Outline each blood parasite and name the species.
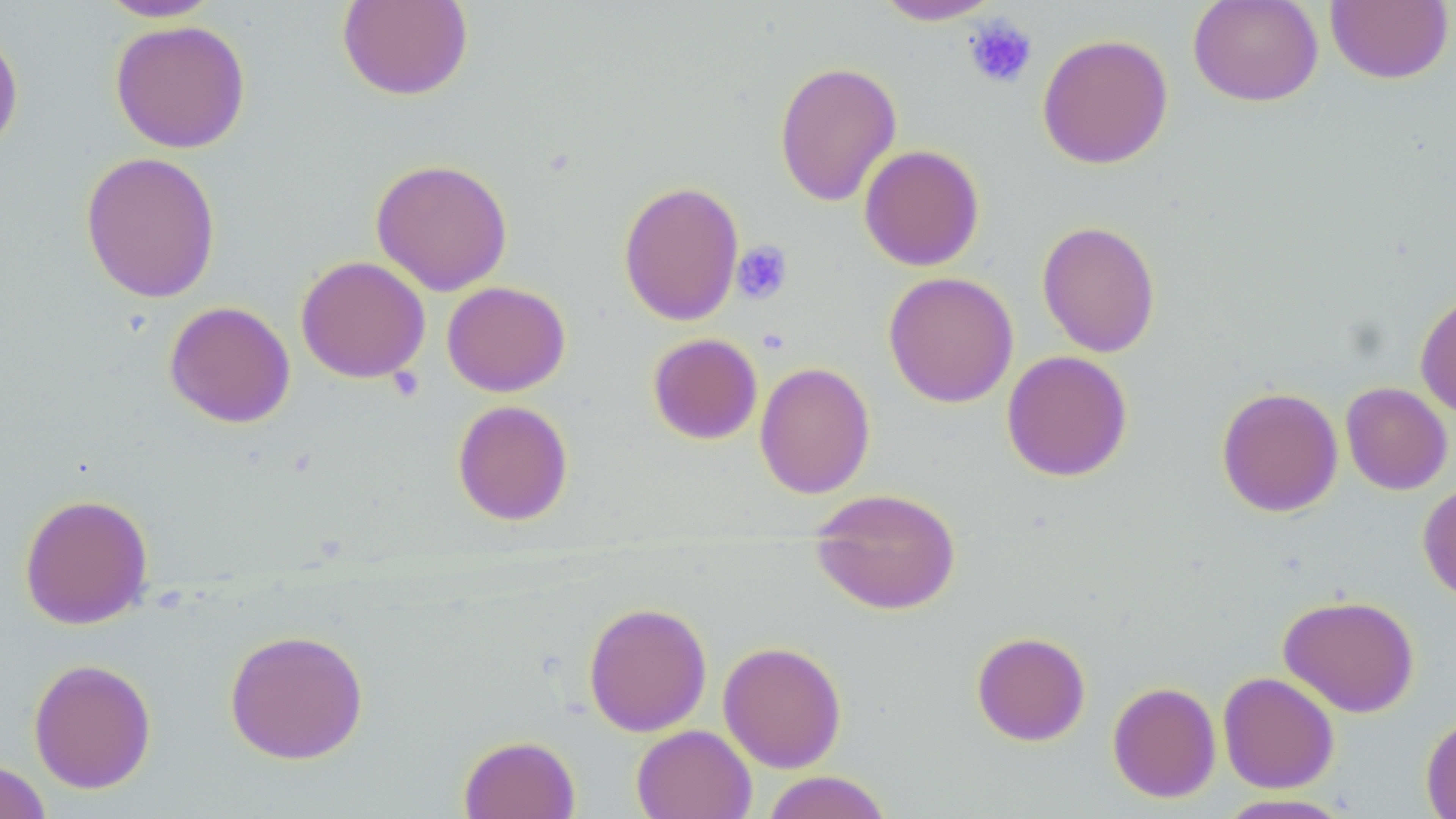

No blood parasites seen.

slide_level_diagnosis: no evidence of blood parasites
stain: May-Grünwald-Giemsa
field_of_view: one of a larger specimen
magnification: 1000x
uninfected_red_blood_cell_locations: 'approximate bounding boxes as [x1, y1, x2, y2] in pixels: [95, 0, 224, 23], [337, 0, 474, 101], [871, 0, 1005, 25], [1187, 0, 1324, 107], [1325, 0, 1454, 84], [109, 20, 251, 154], [0, 23, 24, 157], [1036, 33, 1174, 170], [774, 60, 902, 207], [859, 144, 985, 272], [80, 150, 221, 303], [370, 157, 513, 296], [618, 180, 744, 326], [1036, 220, 1161, 358], [295, 255, 430, 384], [883, 271, 1019, 408], [442, 281, 570, 397], [1414, 290, 1456, 418], [164, 301, 296, 428], [647, 333, 763, 445], [1001, 350, 1133, 482], [754, 361, 876, 499], [1340, 382, 1453, 495], [1216, 386, 1343, 517], [452, 399, 574, 526], [1417, 480, 1456, 603], [809, 488, 961, 615], [18, 492, 154, 629], [1278, 593, 1420, 717], [583, 601, 712, 737], [224, 627, 369, 765], [971, 631, 1091, 746], [718, 641, 847, 772], [28, 657, 157, 794], [1217, 671, 1340, 793], [1107, 681, 1221, 803], [1420, 713, 1456, 818], [631, 725, 757, 819], [457, 734, 580, 818], [0, 759, 52, 819], [760, 770, 894, 819], [1213, 793, 1356, 818]'
platelet_locations: 'approximate bounding boxes as [x1, y1, x2, y2] in pixels: [963, 14, 1038, 90], [731, 240, 793, 305]'
modality: optical microscopy
preparation: thin blood film
image_size: 1456×819 pixels